State the blood parasite species.
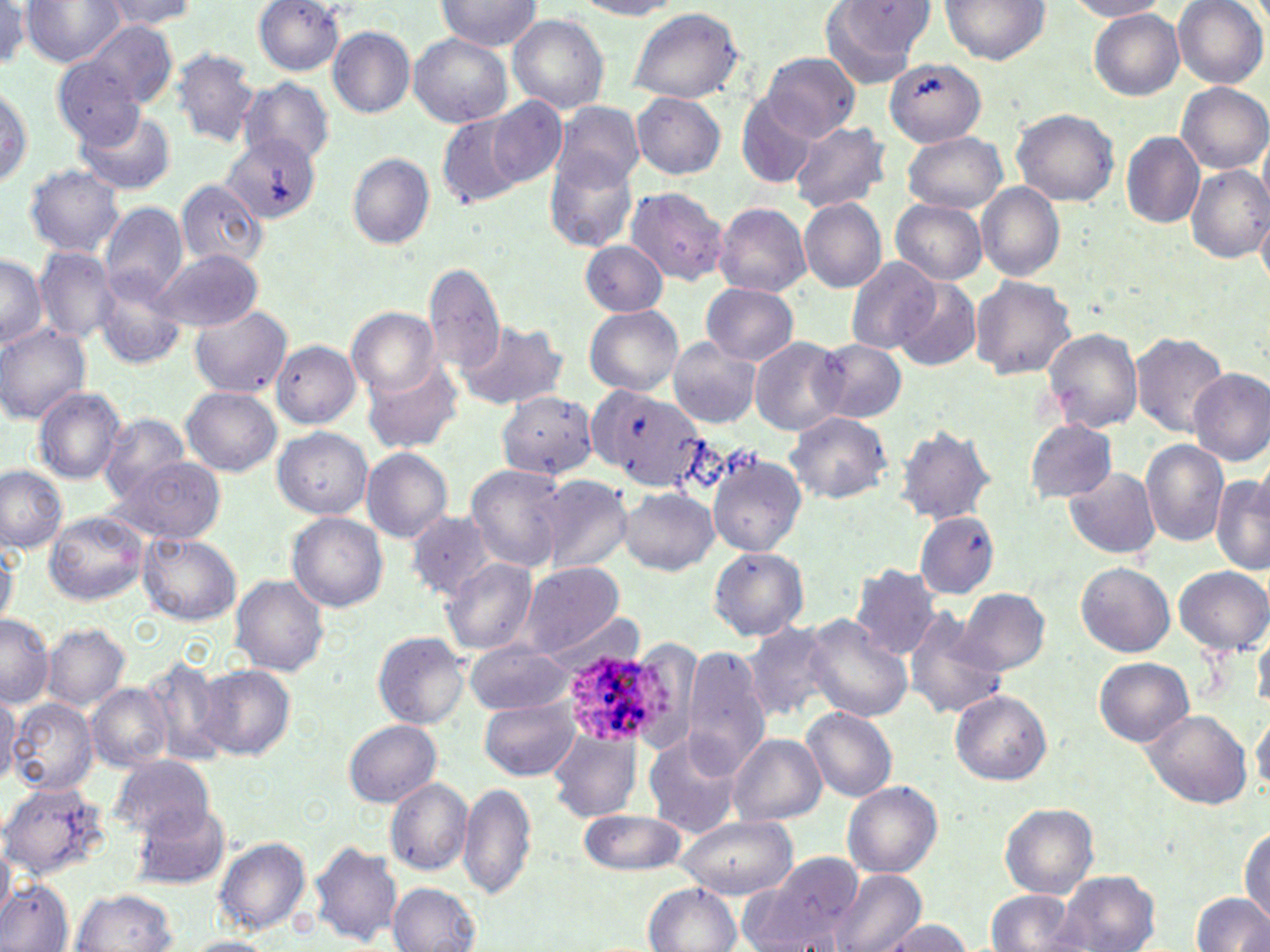
Plasmodium ovale.

Approximate bounding boxes as (x1,y1)-(x2,y2) corner pairs in pixels. Uninfected red blood cell locations: (22,0)-(123,66), (100,0)-(197,32), (434,0)-(543,53), (576,0)-(686,17), (940,0)-(1050,65), (1174,0)-(1269,87), (252,1)-(346,75), (820,1)-(932,84), (1067,1)-(1173,20), (0,4)-(31,72), (626,8)-(745,104), (1090,9)-(1184,100), (509,15)-(610,113), (67,22)-(178,113), (328,27)-(415,117), (408,34)-(513,128), (171,49)-(260,148), (757,53)-(859,142), (886,58)-(988,146), (53,59)-(146,149), (238,77)-(335,165), (0,81)-(32,192), (1176,82)-(1268,174), (735,90)-(824,189), (631,92)-(726,179), (488,97)-(567,187), (551,101)-(644,193), (77,109)-(177,195), (1012,109)-(1119,206), (436,111)-(529,207), (790,121)-(891,214), (902,132)-(1006,213), (1122,132)-(1204,226), (223,135)-(320,223), (546,151)-(641,250), (346,152)-(435,248), (23,164)-(125,257), (1187,165)-(1269,261), (176,180)-(268,268), (976,183)-(1065,280), (625,186)-(729,285), (799,198)-(887,293), (890,198)-(988,285), (713,201)-(811,296), (99,202)-(188,303), (1256,208)-(1270,288), (579,241)-(669,316), (33,247)-(119,344), (152,249)-(264,332), (0,252)-(46,350), (846,257)-(941,356), (425,264)-(505,371), (95,273)-(187,371), (969,275)-(1076,378), (893,279)-(980,371), (701,283)-(799,364), (188,304)-(292,399), (584,305)-(685,395), (346,308)-(441,396), (456,319)-(567,409), (0,325)-(92,423), (1043,329)-(1143,433), (1132,333)-(1227,436), (748,337)-(848,435), (270,339)-(361,428), (668,339)-(760,428), (812,339)-(904,421), (361,359)-(464,454), (1189,368)-(1270,467), (589,383)-(707,488), (32,387)-(126,485), (182,388)-(282,476), (498,390)-(598,481), (785,411)-(892,503), (96,413)-(192,499), (1025,419)-(1117,501), (896,425)-(997,523), (272,427)-(373,518), (1139,440)-(1229,547), (360,448)-(452,542), (707,453)-(806,557), (107,456)-(227,544), (468,464)-(570,570), (0,465)-(68,553), (1066,469)-(1161,558), (1212,474)-(1270,578), (537,475)-(633,574), (621,487)-(717,574), (405,509)-(494,600), (44,512)-(147,606), (288,513)-(388,611), (914,513)-(999,596), (137,532)-(241,626), (0,538)-(18,627), (709,547)-(807,640), (442,558)-(537,658), (516,563)-(624,657), (1077,563)-(1174,657), (850,564)-(944,660), (1172,564)-(1269,654), (230,575)-(329,675), (958,588)-(1051,675), (0,613)-(54,708), (904,614)-(1006,721), (800,615)-(913,723), (738,618)-(839,723), (41,624)-(130,711), (1254,624)-(1270,709), (374,631)-(472,728), (464,640)-(574,715), (605,640)-(699,751), (682,647)-(768,775), (141,657)-(229,766), (1093,657)-(1195,748), (195,664)-(295,759), (88,683)-(172,771), (950,690)-(1052,784), (0,692)-(19,786), (8,699)-(97,796), (480,701)-(582,779), (803,708)-(897,801), (1142,711)-(1252,808), (1251,711)-(1270,796), (343,719)-(442,807), (642,732)-(745,839), (548,734)-(641,821), (728,734)-(826,826), (107,755)-(217,842), (385,779)-(474,876), (0,780)-(111,880), (458,781)-(537,899), (842,781)-(943,878), (131,801)-(230,888), (998,804)-(1099,899), (578,808)-(689,875), (673,815)-(798,899), (1239,827)-(1269,922), (214,837)-(312,935), (0,839)-(14,921), (308,842)-(403,948), (744,852)-(867,950), (832,870)-(927,952), (1052,871)-(1160,952), (0,881)-(73,951), (389,882)-(483,951), (645,883)-(742,952), (71,889)-(181,952), (985,889)-(1080,951), (1192,893)-(1270,951), (879,919)-(975,951), (183,935)-(273,952). Plasmodium ovale-infected red blood cell locations: (566,651)-(676,747). Thin blood smear. Image is 1270×952 pixels. Optical microscopy. 1000x magnification. May-Grünwald-Giemsa-stained preparation. One field of a larger specimen.